Assess this cell for malaria.
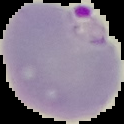

Parasitized.

Cell region segmented out of the field of view; the surrounding area is masked to black. From a thin blood smear. Image is 124×124 pixels.